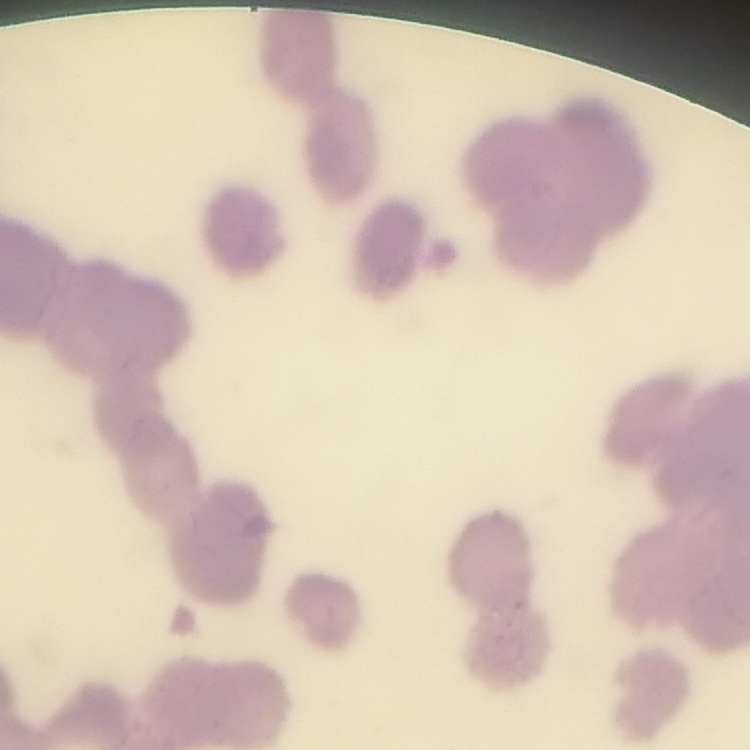

Summary:
  - Red blood cell morphology: rouleaux formation
  - Image type: one tile cut from a larger photomicrograph
  - Stain: Field's or Giemsa
  - Preparation: thin blood smear